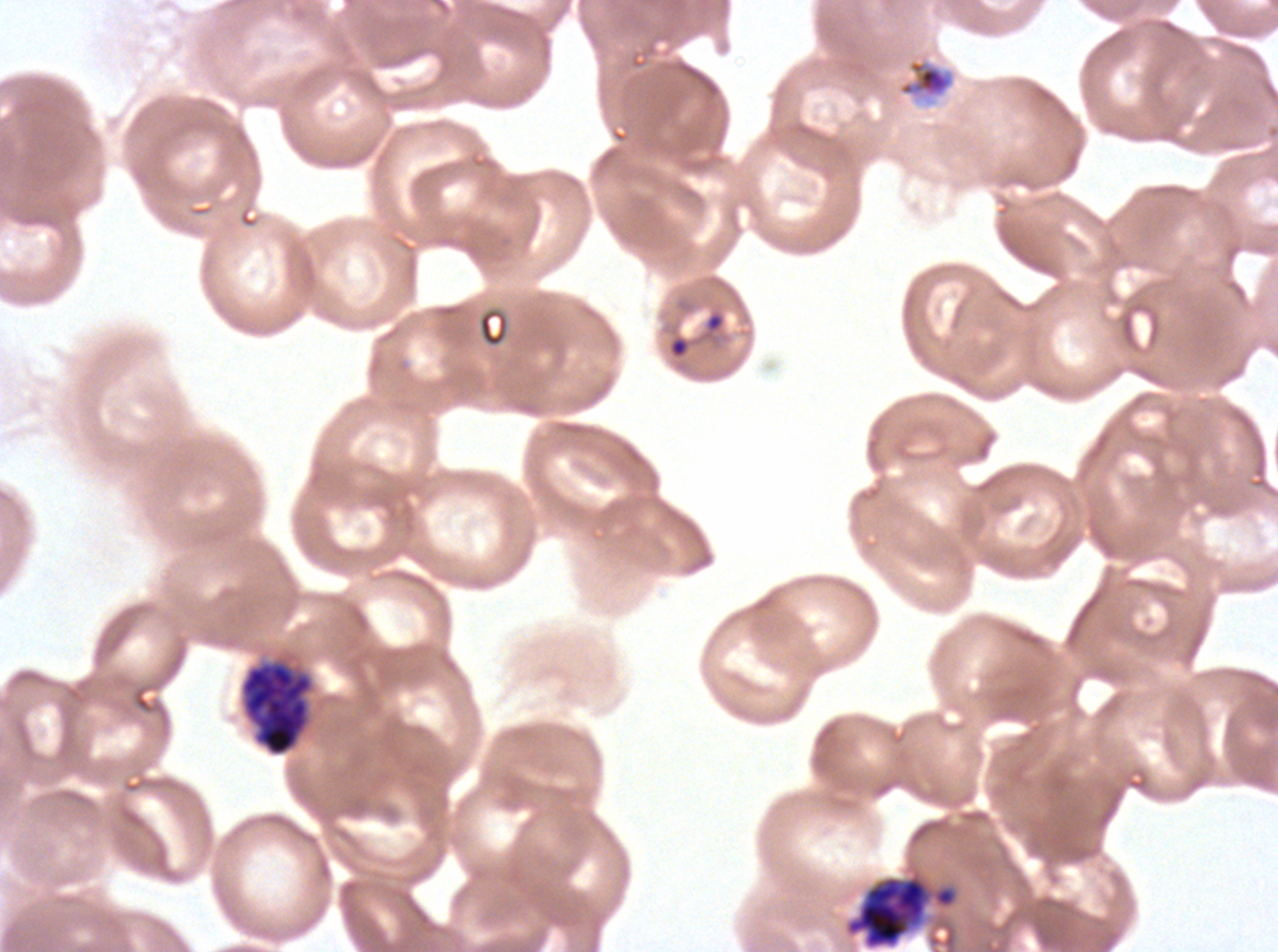
Approximate bounding rectangles given as corner coordinates in pixels from the top-left.
Summary:
  - Early schizont locations: (x1=846, y1=876, x2=929, y2=948)
  - Late schizont locations: (x1=240, y1=660, x2=313, y2=757)
  - Ring locations: (x1=666, y1=307, x2=727, y2=361)
  - Late-ring/early-trophozoite locations: (x1=896, y1=57, x2=956, y2=105)
  - Life-cycle stages observed: ring, late-ring/early-trophozoite, early schizont, late schizont
  - Stain: Giemsa
  - Preparation: thin blood smear
  - Specimen: P. falciparum from a patient in The Gambia, cultured ex vivo for 24 to 48 hours
  - Field of view: one sub-image of a larger composite
  - Image size: 1278×952 pixels